Report the malaria status of this cell.
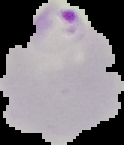

Parasitized.

image type = segmented cell region with the area outside set to black
image size = 124×145 pixels
preparation = thin blood smear